Assess the morphology of the erythrocytes.
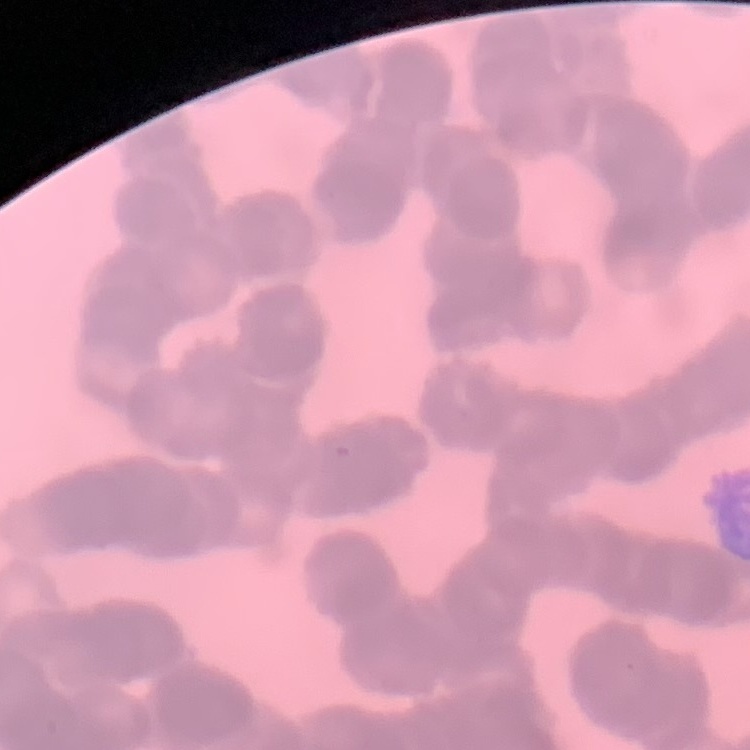

Rouleaux formation.

Stained with either Field's or Giemsa. Square crop of a larger photomicrograph. Thin blood film.